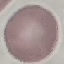
Result: no malaria parasites seen. Giemsa stain. Automatically extracted cell patch, resized to 64 × 64 pixels. Thin smear of blood. Photographed with a smartphone camera at the microscope eyepiece.